Locate and identify every blood parasite.
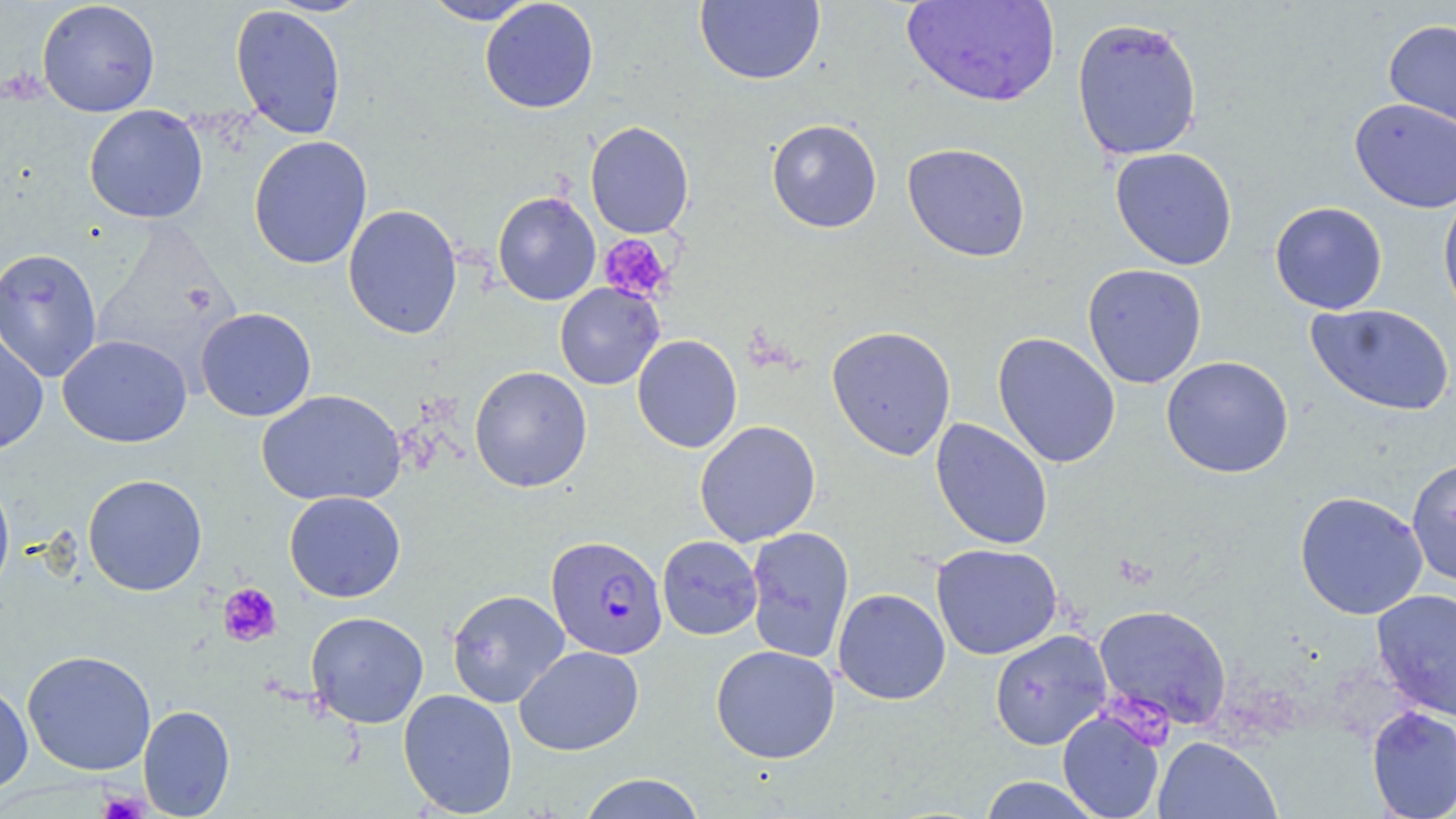
Approximate bounding boxes as (x1,y1)-(x2,y2) corner pairs in pixels.
Plasmodium falciparum-infected red blood cells: (546,535)-(668,660).
No Plasmodium ovale, Plasmodium malariae, Plasmodium vivax, Babesia divergens, or Trypanosoma brucei observed.

Summary:
  - Uninfected red blood cell locations: (37,0)-(160,117), (479,0)-(599,114), (694,0)-(826,86), (421,1)-(539,25), (901,1)-(1059,107), (230,4)-(347,140), (1071,16)-(1203,161), (1383,18)-(1456,133), (1349,97)-(1456,213), (84,104)-(209,224), (766,119)-(882,233), (585,121)-(695,239), (248,135)-(373,270), (902,142)-(1031,262), (1110,147)-(1238,270), (1438,187)-(1456,324), (492,192)-(601,306), (1269,201)-(1388,315), (343,204)-(463,339), (0,247)-(103,382), (1082,263)-(1207,389), (555,283)-(665,390), (1305,303)-(1454,416), (195,307)-(317,422), (0,323)-(49,455), (826,325)-(957,461), (992,332)-(1121,468), (58,334)-(192,448), (632,334)-(742,453), (1161,356)-(1294,478), (469,366)-(592,493), (257,389)-(406,508), (930,417)-(1053,550), (694,420)-(821,547), (1406,457)-(1456,587), (0,473)-(15,602), (83,474)-(208,596), (1294,490)-(1428,620), (284,491)-(406,603), (745,526)-(855,664), (657,535)-(762,640), (931,543)-(1063,660), (832,588)-(951,705), (446,589)-(569,708), (1370,589)-(1456,722), (1093,604)-(1232,730), (305,611)-(429,728), (990,629)-(1112,751), (514,645)-(644,755), (711,645)-(840,763), (22,649)-(156,776), (0,682)-(33,797), (398,689)-(518,817), (138,704)-(235,818), (1366,706)-(1456,818), (1057,709)-(1166,819), (1152,736)-(1282,819), (577,773)-(707,818), (978,776)-(1102,818)
  - Platelet locations: (599,234)-(674,304), (217,583)-(282,647), (1105,690)-(1177,752), (99,788)-(148,819)
  - Slide-level diagnosis: Plasmodium falciparum
  - Modality: light microscopy
  - Stain: May-Grünwald-Giemsa
  - Image size: 1456×819 pixels
  - Preparation: thin blood smear
  - Field of view: single
  - Magnification: 1000x